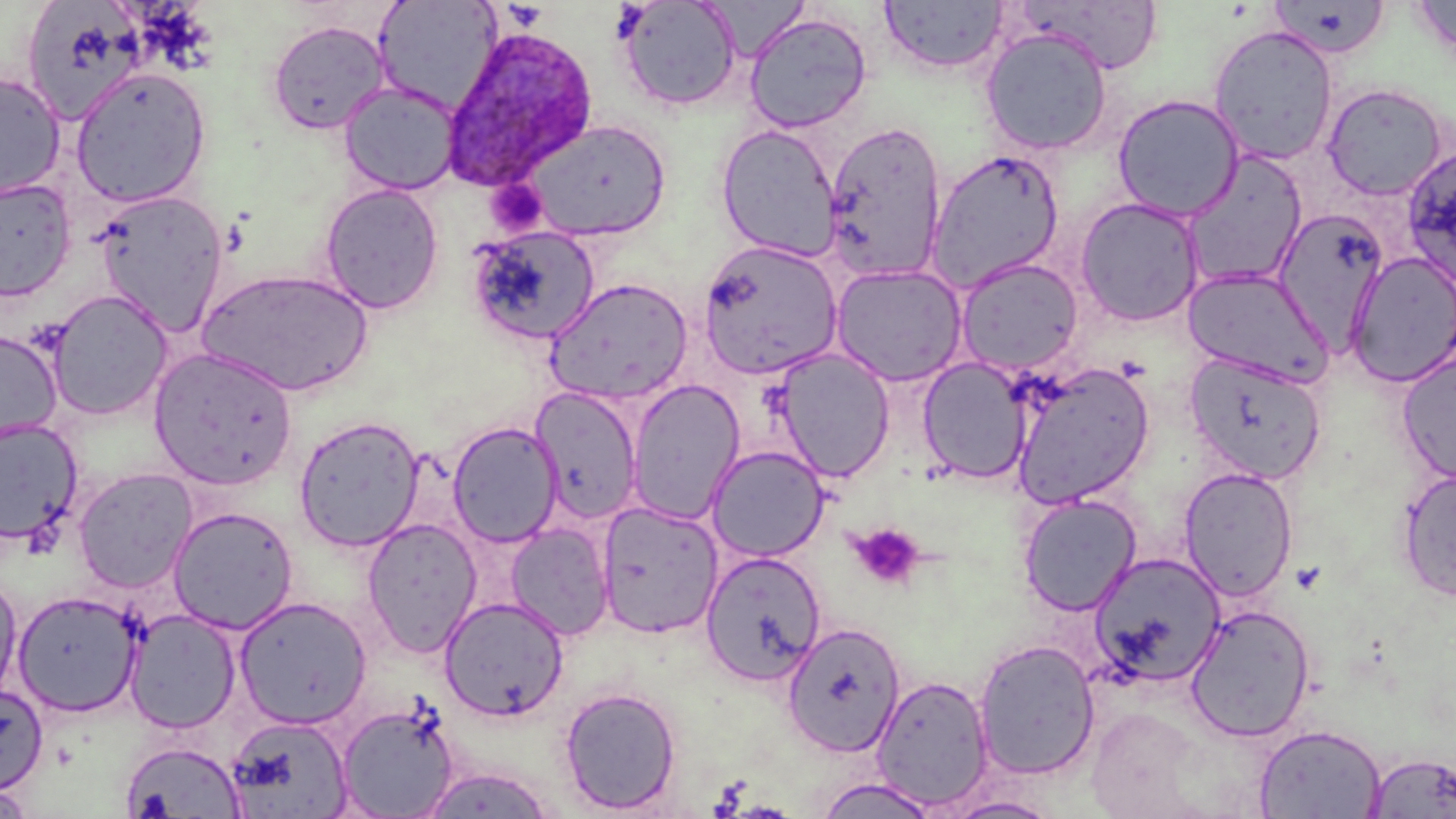

slide-level diagnosis = Plasmodium ovale
modality = light microscopy
image size = 1456×819 pixels
uninfected red blood cell locations = approximate bounding boxes as named x1/y1/x2/y2 corners in pixels: (x1=373, y1=0, x2=502, y2=114), (x1=615, y1=0, x2=743, y2=111), (x1=1017, y1=0, x2=1167, y2=74), (x1=1409, y1=0, x2=1456, y2=66), (x1=878, y1=1, x2=1009, y2=75), (x1=1268, y1=1, x2=1390, y2=59), (x1=25, y1=2, x2=145, y2=125), (x1=744, y1=12, x2=872, y2=133), (x1=267, y1=19, x2=391, y2=135), (x1=1207, y1=24, x2=1340, y2=165), (x1=980, y1=27, x2=1113, y2=156), (x1=70, y1=67, x2=211, y2=207), (x1=0, y1=71, x2=66, y2=200), (x1=339, y1=81, x2=461, y2=195), (x1=1320, y1=82, x2=1450, y2=201), (x1=1111, y1=94, x2=1245, y2=221), (x1=522, y1=118, x2=672, y2=242), (x1=824, y1=119, x2=948, y2=283), (x1=715, y1=123, x2=844, y2=262), (x1=1402, y1=144, x2=1456, y2=286), (x1=927, y1=149, x2=1063, y2=291), (x1=1182, y1=151, x2=1308, y2=291), (x1=0, y1=177, x2=77, y2=302), (x1=319, y1=183, x2=444, y2=314), (x1=93, y1=189, x2=229, y2=335), (x1=1075, y1=196, x2=1206, y2=328), (x1=1274, y1=209, x2=1390, y2=350), (x1=465, y1=225, x2=601, y2=345), (x1=697, y1=240, x2=843, y2=380), (x1=1346, y1=252, x2=1456, y2=385), (x1=956, y1=257, x2=1083, y2=375), (x1=830, y1=263, x2=967, y2=387), (x1=1182, y1=266, x2=1334, y2=387), (x1=196, y1=267, x2=374, y2=397), (x1=544, y1=277, x2=693, y2=406), (x1=46, y1=290, x2=174, y2=421), (x1=0, y1=330, x2=63, y2=445), (x1=771, y1=347, x2=896, y2=482), (x1=149, y1=348, x2=298, y2=490), (x1=1396, y1=350, x2=1456, y2=485), (x1=1185, y1=351, x2=1327, y2=484), (x1=917, y1=357, x2=1033, y2=484), (x1=1009, y1=361, x2=1155, y2=508), (x1=625, y1=378, x2=745, y2=525), (x1=531, y1=386, x2=643, y2=525), (x1=293, y1=415, x2=425, y2=552), (x1=0, y1=418, x2=83, y2=544), (x1=447, y1=421, x2=564, y2=547), (x1=707, y1=445, x2=829, y2=562), (x1=72, y1=467, x2=198, y2=594), (x1=1178, y1=467, x2=1299, y2=601), (x1=1396, y1=468, x2=1456, y2=602), (x1=1018, y1=493, x2=1142, y2=616), (x1=596, y1=501, x2=723, y2=639), (x1=167, y1=506, x2=299, y2=634), (x1=361, y1=518, x2=483, y2=657), (x1=505, y1=522, x2=614, y2=641), (x1=700, y1=551, x2=826, y2=684), (x1=1088, y1=552, x2=1226, y2=687), (x1=0, y1=573, x2=23, y2=707), (x1=12, y1=589, x2=143, y2=717), (x1=234, y1=596, x2=372, y2=729), (x1=440, y1=596, x2=568, y2=721), (x1=1184, y1=604, x2=1316, y2=742), (x1=124, y1=608, x2=242, y2=734), (x1=781, y1=622, x2=906, y2=757), (x1=973, y1=639, x2=1101, y2=780), (x1=871, y1=674, x2=994, y2=811), (x1=0, y1=682, x2=49, y2=795), (x1=559, y1=686, x2=682, y2=814), (x1=336, y1=700, x2=461, y2=818), (x1=225, y1=715, x2=353, y2=817), (x1=1254, y1=723, x2=1386, y2=819), (x1=120, y1=740, x2=247, y2=817), (x1=1363, y1=751, x2=1456, y2=818), (x1=416, y1=767, x2=557, y2=818), (x1=812, y1=776, x2=940, y2=819), (x1=0, y1=784, x2=38, y2=818), (x1=942, y1=795, x2=1063, y2=818)
preparation = thin blood smear
stain = May-Grünwald-Giemsa
field of view = one of a larger specimen
platelet locations = approximate bounding boxes as named x1/y1/x2/y2 corners in pixels: (x1=484, y1=180, x2=551, y2=235), (x1=848, y1=522, x2=925, y2=591)
Plasmodium ovale-infected red blood cell locations = approximate bounding boxes as named x1/y1/x2/y2 corners in pixels: (x1=440, y1=24, x2=600, y2=191)
magnification = 1000x